State which parasite is depicted.
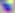

Toxoplasma gondii.

Summary:
  - Magnification: 400x
  - Modality: micrograph